Report the malaria status of this cell.
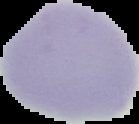

Uninfected.

preparation = thin blood film
image size = 139×124 pixels
image type = cell region segmented out of the field of view; surrounding area masked to black